Describe the morphology of the erythrocytes.
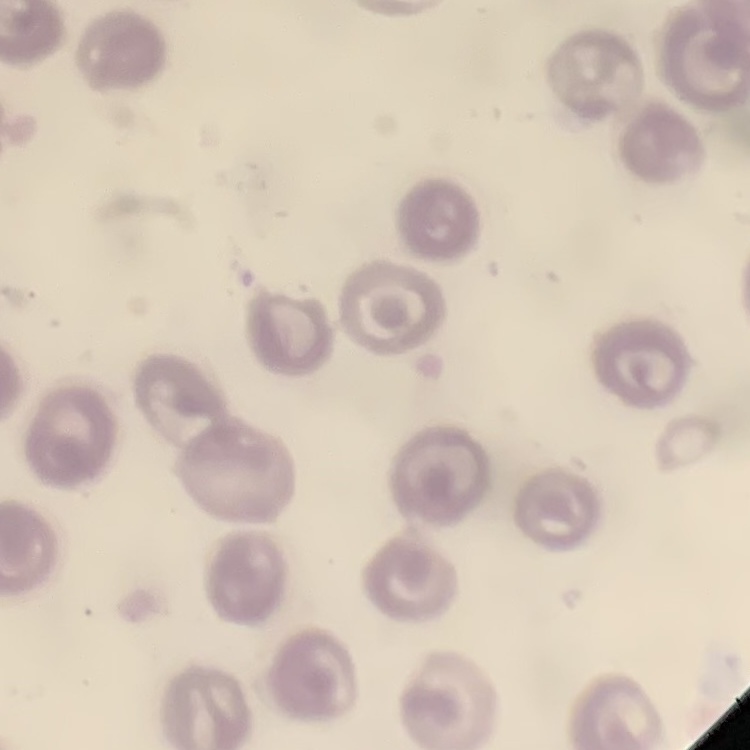
No rouleaux formation.

Summary:
  - Preparation: thin blood smear
  - Image type: square crop of a larger photomicrograph
  - Stain: Field's or Giemsa